Report the malaria status of this cell.
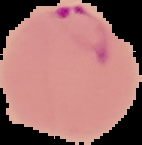

Parasitized.

image size = 142×145 pixels
preparation = thin blood film
image type = segmented cell region on a black background